Mark where platelets are.
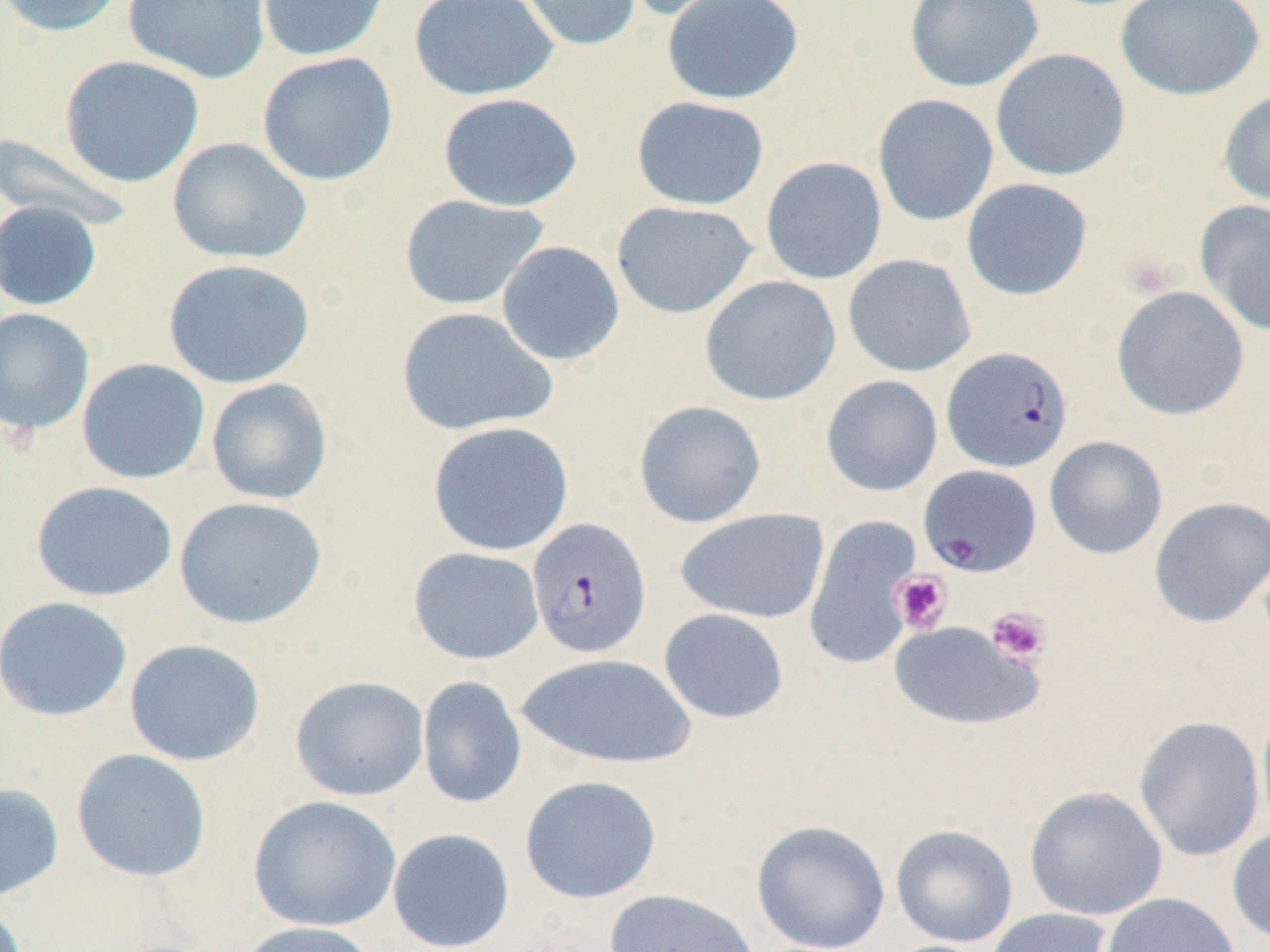
Approximate bounding boxes as named x1/y1/x2/y2 corners in pixels.
Platelets: (x1=890, y1=570, x2=953, y2=634), (x1=985, y1=606, x2=1051, y2=667).

Uninfected red blood cell locations: (x1=0, y1=0, x2=126, y2=38), (x1=123, y1=0, x2=271, y2=84), (x1=256, y1=0, x2=390, y2=62), (x1=408, y1=0, x2=558, y2=102), (x1=513, y1=0, x2=642, y2=52), (x1=621, y1=0, x2=757, y2=22), (x1=662, y1=0, x2=804, y2=105), (x1=903, y1=0, x2=1044, y2=92), (x1=1115, y1=0, x2=1265, y2=101), (x1=990, y1=48, x2=1130, y2=181), (x1=257, y1=52, x2=399, y2=186), (x1=59, y1=55, x2=204, y2=188), (x1=1219, y1=88, x2=1270, y2=208), (x1=438, y1=92, x2=583, y2=212), (x1=872, y1=94, x2=999, y2=227), (x1=631, y1=96, x2=770, y2=211), (x1=0, y1=132, x2=133, y2=231), (x1=167, y1=136, x2=312, y2=265), (x1=760, y1=156, x2=887, y2=284), (x1=961, y1=178, x2=1093, y2=301), (x1=398, y1=194, x2=550, y2=311), (x1=0, y1=200, x2=102, y2=311), (x1=1194, y1=200, x2=1270, y2=336), (x1=611, y1=201, x2=758, y2=319), (x1=495, y1=241, x2=625, y2=366), (x1=842, y1=253, x2=976, y2=378), (x1=162, y1=258, x2=316, y2=389), (x1=699, y1=275, x2=841, y2=406), (x1=1111, y1=285, x2=1250, y2=421), (x1=395, y1=306, x2=558, y2=437), (x1=0, y1=307, x2=95, y2=436), (x1=76, y1=358, x2=210, y2=485), (x1=821, y1=375, x2=943, y2=497), (x1=205, y1=378, x2=333, y2=506), (x1=633, y1=400, x2=767, y2=528), (x1=427, y1=421, x2=574, y2=556), (x1=1044, y1=436, x2=1168, y2=560), (x1=30, y1=480, x2=178, y2=602), (x1=173, y1=496, x2=328, y2=630), (x1=1148, y1=496, x2=1270, y2=628), (x1=674, y1=508, x2=829, y2=625), (x1=804, y1=515, x2=923, y2=670), (x1=408, y1=547, x2=544, y2=665), (x1=0, y1=595, x2=133, y2=722), (x1=658, y1=608, x2=789, y2=724), (x1=887, y1=620, x2=1041, y2=731), (x1=123, y1=638, x2=266, y2=767), (x1=517, y1=653, x2=697, y2=769), (x1=417, y1=675, x2=527, y2=809), (x1=290, y1=676, x2=430, y2=801), (x1=1256, y1=701, x2=1270, y2=837), (x1=1134, y1=714, x2=1266, y2=863), (x1=71, y1=748, x2=211, y2=882), (x1=519, y1=774, x2=662, y2=904), (x1=0, y1=782, x2=65, y2=902), (x1=1024, y1=786, x2=1168, y2=921), (x1=247, y1=795, x2=402, y2=932), (x1=751, y1=820, x2=891, y2=952), (x1=890, y1=824, x2=1019, y2=948), (x1=1226, y1=825, x2=1270, y2=945), (x1=387, y1=828, x2=516, y2=952), (x1=604, y1=888, x2=761, y2=952), (x1=1101, y1=892, x2=1242, y2=952), (x1=0, y1=897, x2=29, y2=952), (x1=984, y1=907, x2=1115, y2=952), (x1=233, y1=921, x2=380, y2=952). Plasmodium falciparum-infected red blood cell locations: (x1=942, y1=346, x2=1074, y2=473), (x1=918, y1=464, x2=1042, y2=576), (x1=527, y1=518, x2=652, y2=659). Slide-level diagnosis: Plasmodium falciparum. Thin blood film. 1000x magnification. One field of a larger specimen. Light microscopy. May-Grünwald-Giemsa-stained preparation. Image is 1270×952 pixels.